Identify the cell.
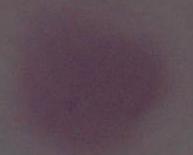

An erythrocyte.

Photomicrograph. 1000x magnification.